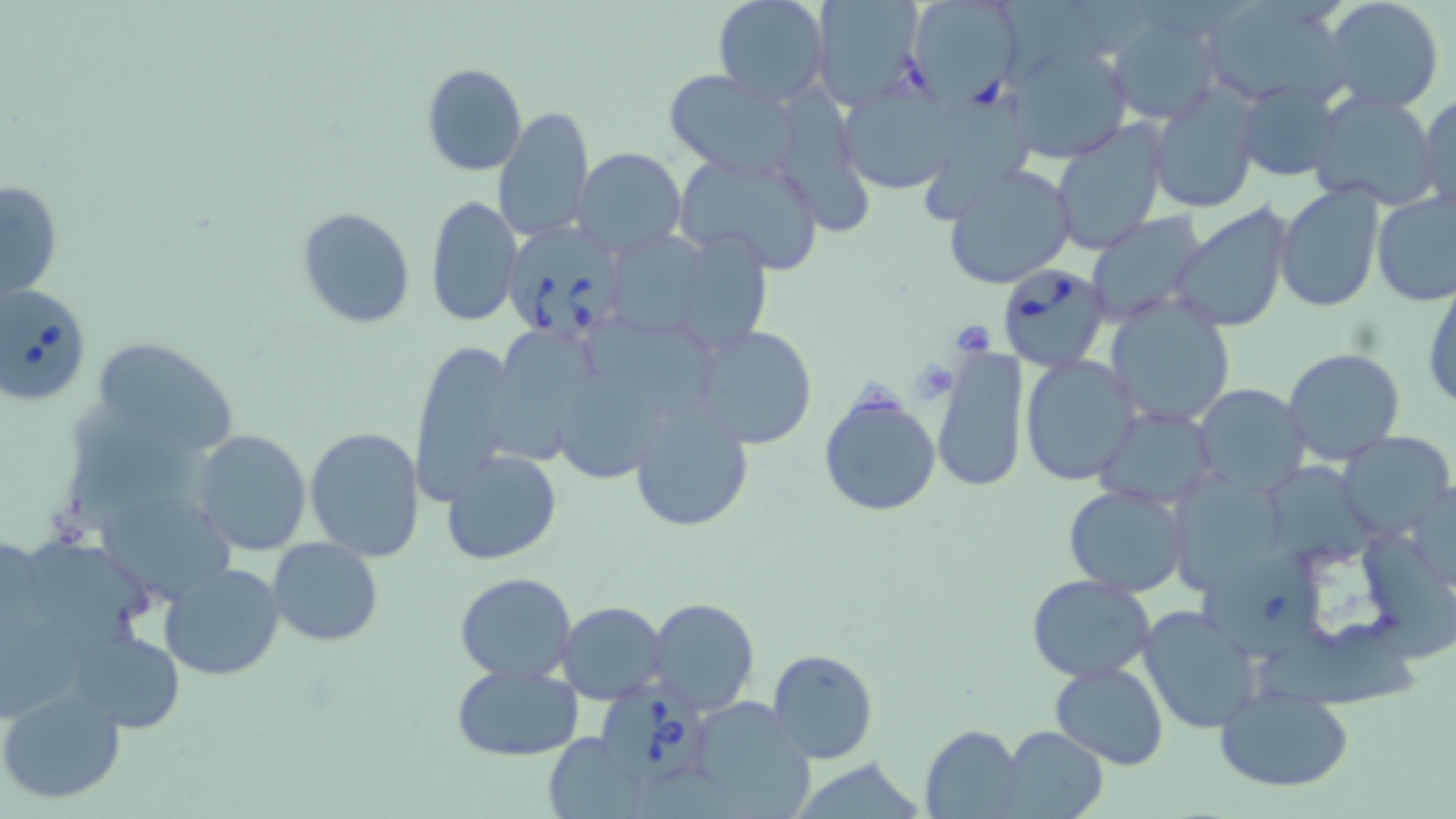
Summary:
  - Coordinate format: approximate bounding boxes as [x1, y1, x2, y2] in pixels
  - Uninfected red blood cell locations: [713, 0, 831, 107], [808, 0, 926, 109], [905, 0, 1025, 109], [1199, 0, 1346, 105], [1321, 0, 1445, 115], [1105, 11, 1224, 125], [1007, 44, 1134, 163], [422, 64, 527, 177], [663, 70, 802, 180], [1234, 80, 1344, 183], [835, 82, 962, 195], [1148, 87, 1262, 214], [1306, 89, 1443, 211], [1417, 93, 1455, 210], [922, 99, 1030, 216], [492, 105, 595, 243], [1050, 120, 1169, 256], [574, 146, 685, 257], [672, 148, 826, 273], [942, 162, 1077, 290], [3, 175, 63, 306], [1274, 185, 1385, 312], [1372, 190, 1456, 306], [426, 194, 521, 327], [1169, 203, 1294, 334], [296, 206, 416, 329], [1085, 213, 1210, 327], [680, 228, 778, 353], [619, 237, 725, 339], [1423, 277, 1456, 416], [1105, 298, 1235, 426], [580, 315, 728, 414], [692, 324, 817, 449], [499, 327, 603, 469], [98, 340, 239, 456], [410, 343, 522, 503], [932, 348, 1030, 492], [1281, 348, 1405, 466], [1020, 354, 1141, 485], [552, 369, 668, 483], [1191, 384, 1311, 494], [818, 388, 942, 518], [625, 395, 756, 535], [61, 407, 213, 537], [1094, 407, 1217, 508], [304, 426, 425, 561], [191, 429, 311, 556], [1338, 431, 1455, 539], [441, 449, 562, 565], [1273, 468, 1373, 580], [1178, 470, 1296, 593], [1405, 480, 1454, 593], [1063, 484, 1189, 596], [88, 500, 259, 605], [1361, 523, 1456, 668], [26, 537, 167, 636], [268, 538, 384, 646], [1200, 555, 1331, 671], [158, 562, 287, 680], [453, 571, 578, 683], [1027, 576, 1154, 681], [648, 597, 759, 714], [557, 600, 665, 704], [1137, 604, 1262, 734], [1262, 618, 1419, 724], [69, 629, 184, 735], [769, 649, 877, 763], [1050, 660, 1168, 770], [451, 662, 582, 763], [0, 684, 126, 806], [1213, 685, 1355, 792], [681, 699, 819, 819], [920, 726, 1023, 816], [999, 726, 1109, 818], [544, 732, 648, 817]
  - Babesia divergens-infected red blood cell locations: [503, 222, 631, 343], [996, 262, 1110, 371], [0, 285, 92, 409], [592, 677, 714, 786]
  - Slide-level diagnosis: Babesia divergens
  - Stain: May-Grünwald-Giemsa
  - Preparation: thin blood film
  - Image size: 1456×819 pixels
  - Magnification: 1000x
  - Field of view: one of a larger specimen
  - Modality: optical microscopy